Assess this cell for malaria.
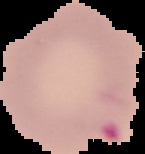

Parasitized.

Summary:
  - Image size: 145×154 pixels
  - Image type: cell region segmented out of the field of view; surrounding area masked to black
  - Preparation: thin blood film